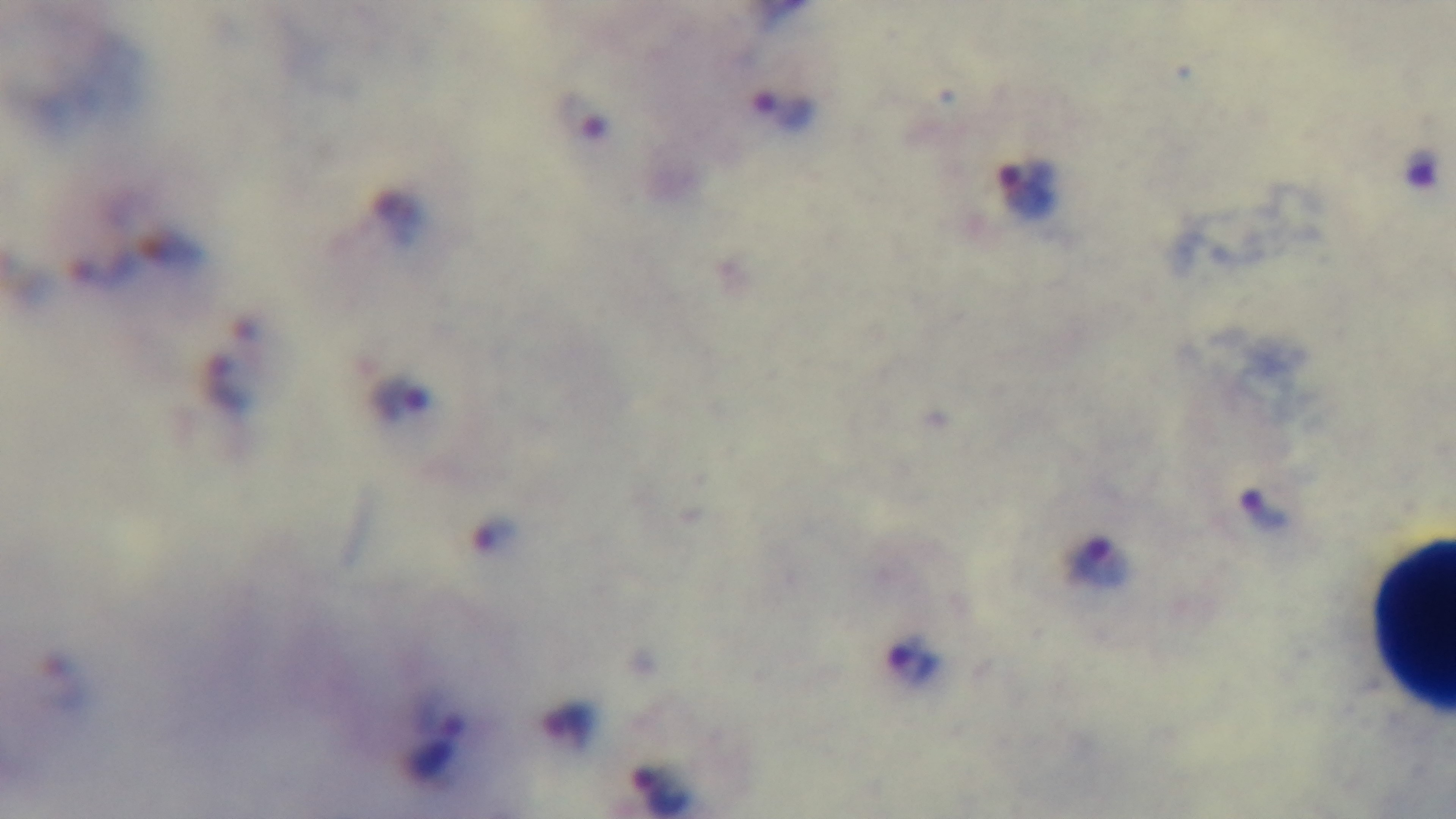

{
  "stain": "Giemsa",
  "objective": "100x oil immersion",
  "field_of_view": "one from the slide",
  "preparation": "thick blood film",
  "malaria_status": "infected",
  "modality": "light microscopy",
  "capture": "mounted 4K digital camera"
}